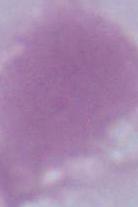 A red blood cell is shown. 1000x magnification. Micrograph.